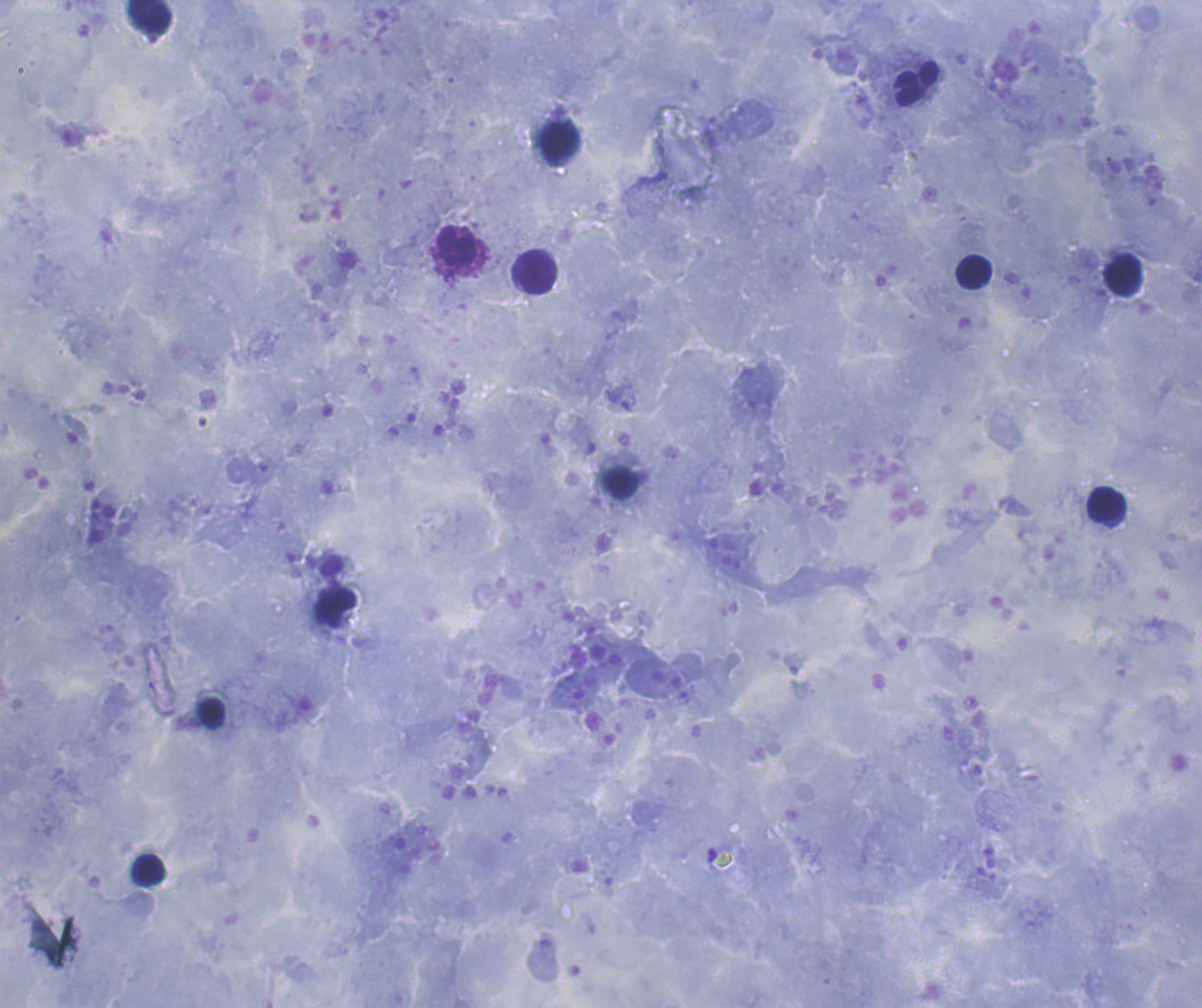
Approximate object centers, in pixels from the top-left corner. Leukocyte locations: (x=148, y=16), (x=916, y=84), (x=561, y=140), (x=458, y=245), (x=535, y=272), (x=974, y=272), (x=1124, y=275), (x=621, y=483), (x=1107, y=505), (x=212, y=713), (x=148, y=871). Coloration quality: good. Previously used in a real diagnosis. Thick blood smear. Romanowsky-stained preparation. Result: no malaria parasites seen. Single field of view. Image is 1202×1008 pixels. Background quality: satisfactory. Captured at 100x magnification.